State which parasite is depicted.
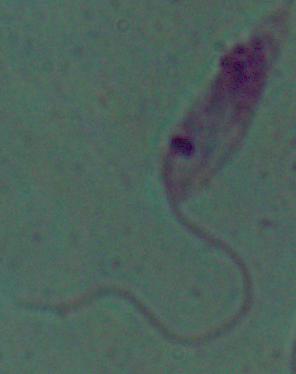

This is Leishmania.

modality: micrograph
magnification: 1000x